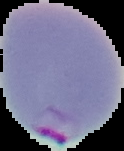
{
  "image_size": "124×151 pixels",
  "malaria_status": "parasitized",
  "preparation": "thin blood film",
  "image_type": "cell region segmented out of the field of view; surrounding area masked to black"
}